Report the malaria status of this cell.
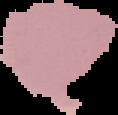

It is uninfected.

preparation: thin blood smear
image_size: 118×115 pixels
image_type: segmented cell region on a black background